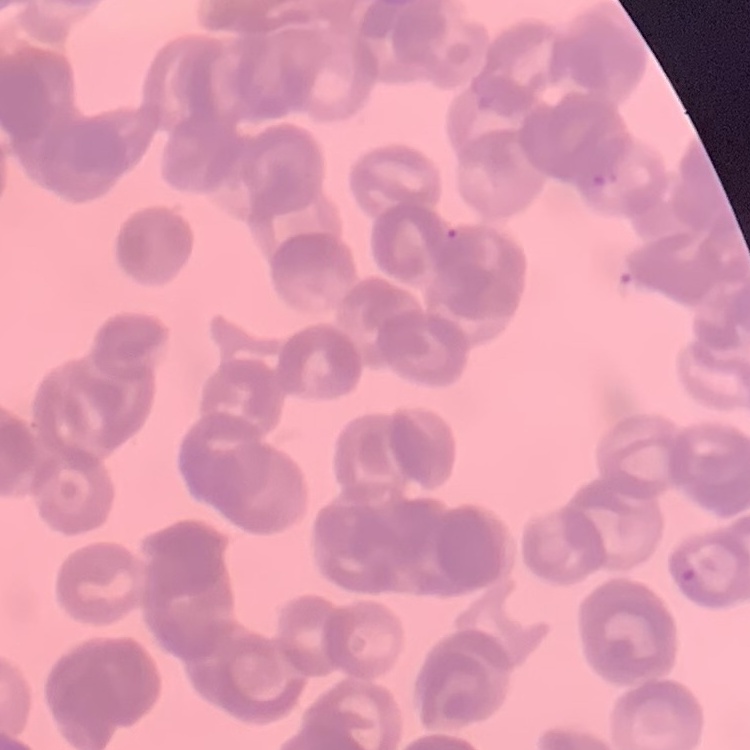

erythrocyte_morphology: rouleaux formation
preparation: thin peripheral smear
stain: Field's or Giemsa
image_type: square crop of a larger photomicrograph